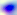
identification = Toxoplasma gondii
modality = photomicrograph
magnification = 400x